Name the parasite shown.
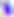

Toxoplasma gondii.

magnification = 400x
modality = micrograph